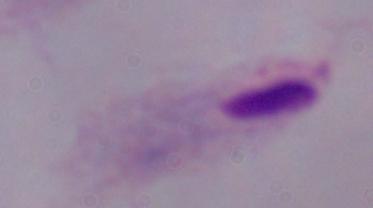 Micrograph. 1000x magnification. A trichomonad is shown.